Describe the morphology of the red blood cells.
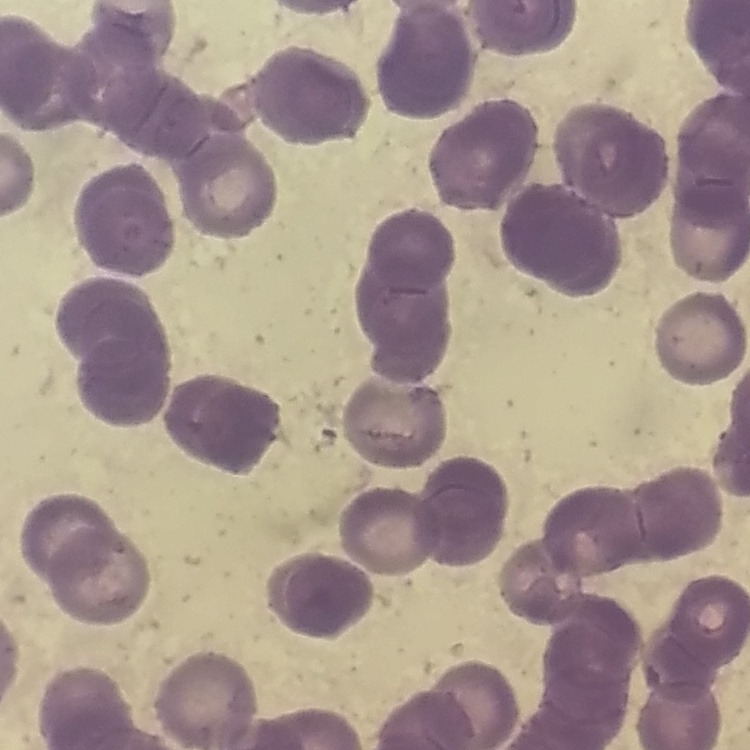

They show rouleaux formation.

Summary:
  - Preparation: thin blood film
  - Image type: square crop of a larger photomicrograph
  - Stain: Field's or Giemsa